Name the parasite shown.
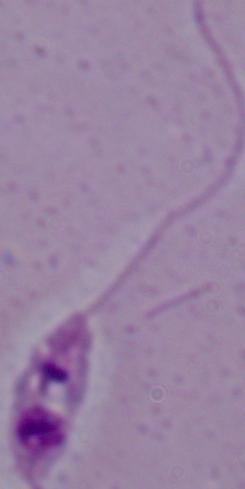
Leishmania.

Micrograph. 1000x magnification.